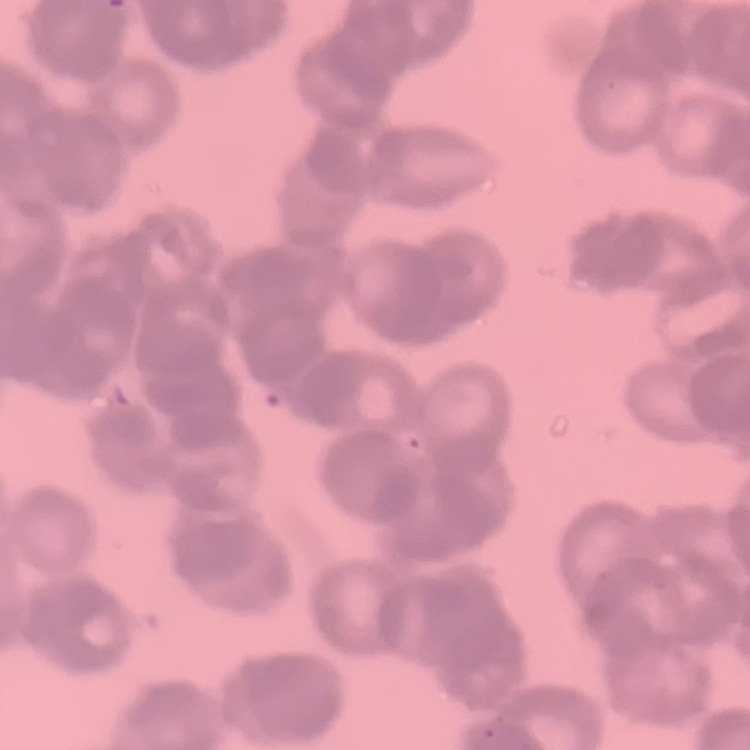 The red blood cells exhibit rouleaux formation. Square crop of a larger photomicrograph. Stained with either Field's or Giemsa. Thin blood smear.